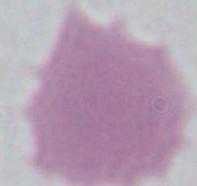
Captured at 1000x magnification. A red blood cell is seen. Photomicrograph.